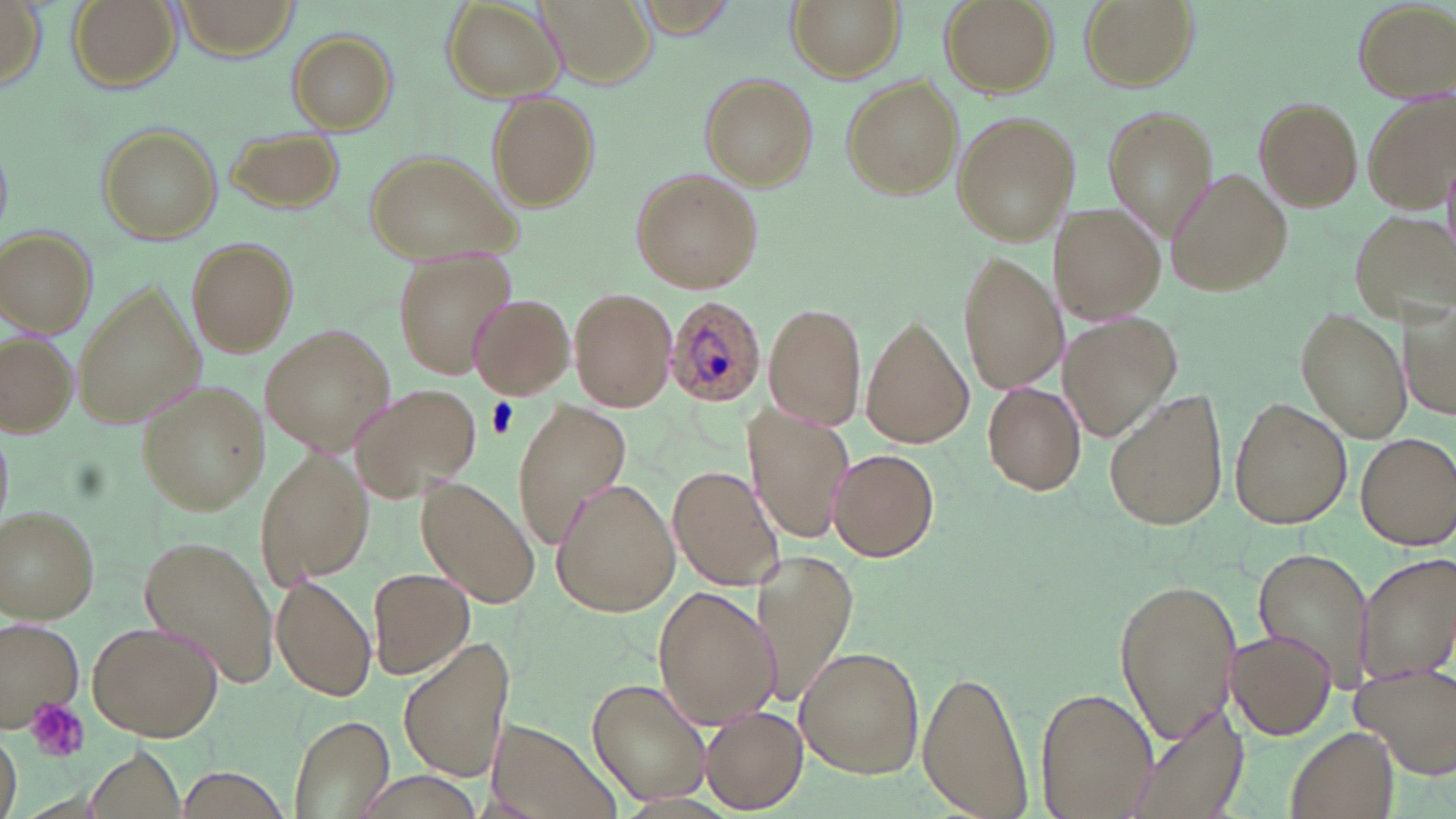

Approximate bounding boxes as (x1, y1, x2, y2) in pixels. Uninfected red blood cell locations: (67, 0, 182, 92), (173, 0, 300, 59), (539, 0, 654, 84), (786, 0, 905, 81), (939, 0, 1056, 97), (1076, 0, 1200, 93), (1, 1, 44, 90), (1352, 1, 1454, 103), (441, 2, 563, 101), (625, 2, 745, 36), (287, 31, 396, 134), (701, 73, 816, 187), (840, 74, 962, 199), (487, 93, 599, 209), (1365, 94, 1453, 211), (1253, 97, 1364, 207), (1101, 107, 1212, 238), (951, 111, 1078, 247), (95, 122, 222, 245), (224, 127, 342, 215), (364, 150, 520, 265), (632, 168, 761, 292), (1166, 168, 1292, 297), (1051, 202, 1165, 325), (1346, 211, 1456, 333), (1, 228, 96, 335), (189, 240, 298, 356), (391, 249, 516, 379), (958, 251, 1065, 396), (74, 285, 201, 429), (569, 288, 678, 411), (1402, 290, 1456, 425), (469, 293, 574, 399), (764, 303, 867, 431), (1298, 309, 1410, 443), (1061, 313, 1180, 441), (861, 318, 973, 451), (260, 327, 395, 455), (1, 334, 77, 436), (981, 381, 1086, 496), (137, 382, 270, 516), (351, 382, 481, 502), (1104, 388, 1229, 534), (1229, 398, 1350, 530), (512, 403, 631, 545), (743, 407, 853, 544), (0, 421, 12, 529), (1357, 432, 1455, 548), (257, 449, 374, 586), (829, 449, 939, 563), (669, 465, 785, 589), (416, 480, 541, 609), (550, 480, 680, 616), (1, 507, 101, 623), (138, 535, 283, 689), (1253, 547, 1377, 692), (756, 551, 859, 711), (1356, 552, 1456, 682), (368, 567, 475, 680), (271, 576, 377, 702), (1112, 576, 1243, 743), (653, 586, 781, 728), (0, 618, 85, 726), (84, 620, 222, 741), (1228, 629, 1336, 740), (400, 642, 515, 784), (795, 647, 924, 778), (1352, 661, 1456, 778), (917, 670, 1029, 817), (588, 677, 712, 807), (1035, 685, 1156, 819), (1121, 701, 1245, 819), (701, 707, 806, 812), (287, 712, 395, 818), (488, 717, 617, 818), (1286, 727, 1399, 819), (1, 734, 20, 819), (88, 748, 187, 819), (179, 766, 290, 817). Platelet locations: (486, 398, 518, 437), (27, 699, 89, 763). Plasmodium ovale-infected red blood cell locations: (663, 295, 767, 408). Slide-level diagnosis: Plasmodium ovale. May-Grünwald-Giemsa-stained preparation. Light microscopy. Captured at 1000x magnification. Image is 1456×819 pixels. Single field of view. Thin blood smear.